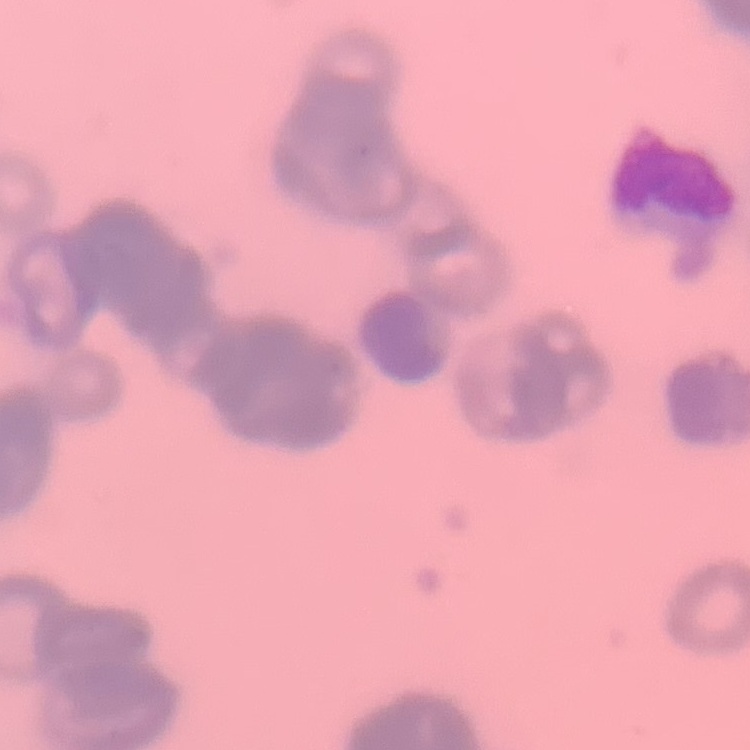
erythrocyte morphology = rouleaux formation
stain = Field's or Giemsa
preparation = thin blood film
image type = square crop of a larger photomicrograph